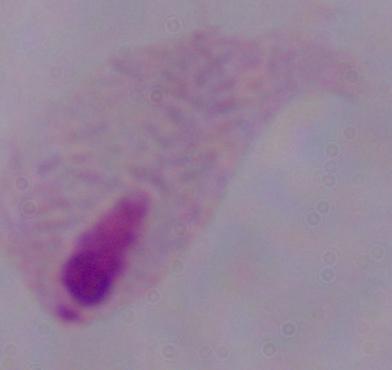
magnification = 1000x
modality = photomicrograph
identification = trichomonad